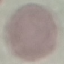

Summary:
  - Malaria status: uninfected
  - Capture: smartphone through the microscope eyepiece
  - Image type: cell patch, automatically extracted from a larger field of view and resized to 64 × 64 pixels
  - Stain: Giemsa
  - Preparation: thin smear